Report the malaria status of this cell.
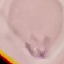

Uninfected.

image type = cell patch, automatically extracted from a larger field of view and resized to 64 × 64 pixels
preparation = thin blood film
stain = Giemsa
capture = smartphone camera at the microscope eyepiece